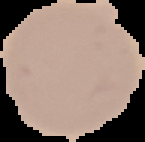

Image is 145×142 pixels. Malaria status: uninfected. The area outside the segmented cell region is set to black. From a thin blood smear.